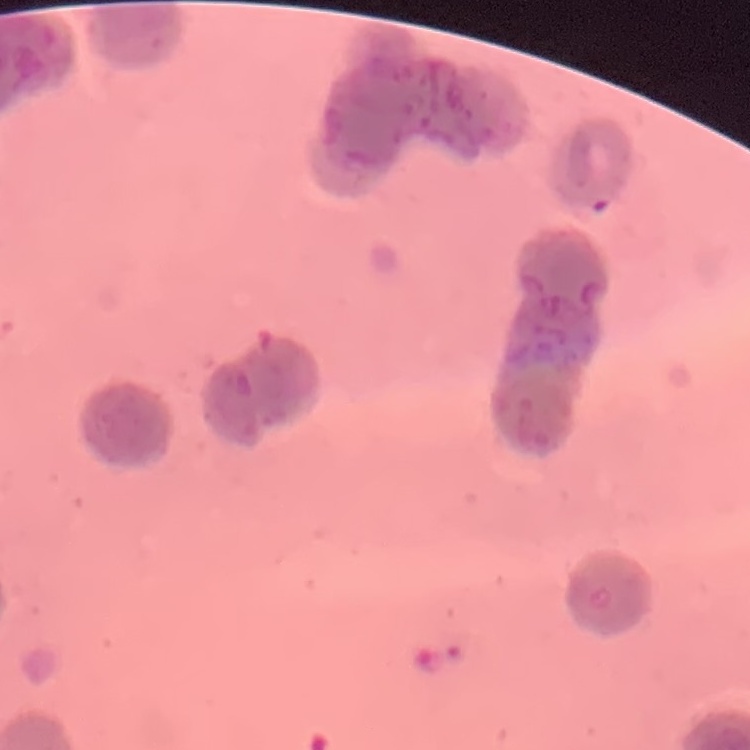
red_blood_cell_morphology: rouleaux formation
image_type: one tile cut from a larger photomicrograph
stain: Field's or Giemsa
preparation: thin blood film